Report the malaria status of this cell.
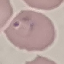
Parasitized.

stain = Giemsa
image type = automatically extracted cell patch, resized to 64 × 64 pixels
capture = smartphone through the microscope eyepiece
preparation = thin blood film